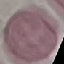
Summary:
  - Malaria status: uninfected
  - Stain: Giemsa
  - Capture: smartphone camera at the microscope eyepiece
  - Preparation: thin smear
  - Image type: cell patch, automatically extracted from a larger field of view and resized to 64 × 64 pixels